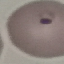

result = malaria parasites identified
preparation = thin blood smear
stain = Giemsa
capture = smartphone camera at the microscope eyepiece
image type = automatically extracted cell patch, resized to 64 × 64 pixels